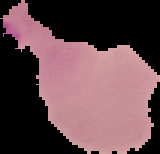

Summary:
  - Image type: segmented cell region with the area outside set to black
  - Malaria status: parasitized
  - Preparation: thin blood film
  - Image size: 160×154 pixels